Assess this cell for malaria.
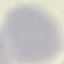
Uninfected.

Thin blood smear. Cell patch, automatically extracted from a larger field of view and resized to 64 × 64 pixels. Acquired by smartphone through the microscope eyepiece. Giemsa stain.